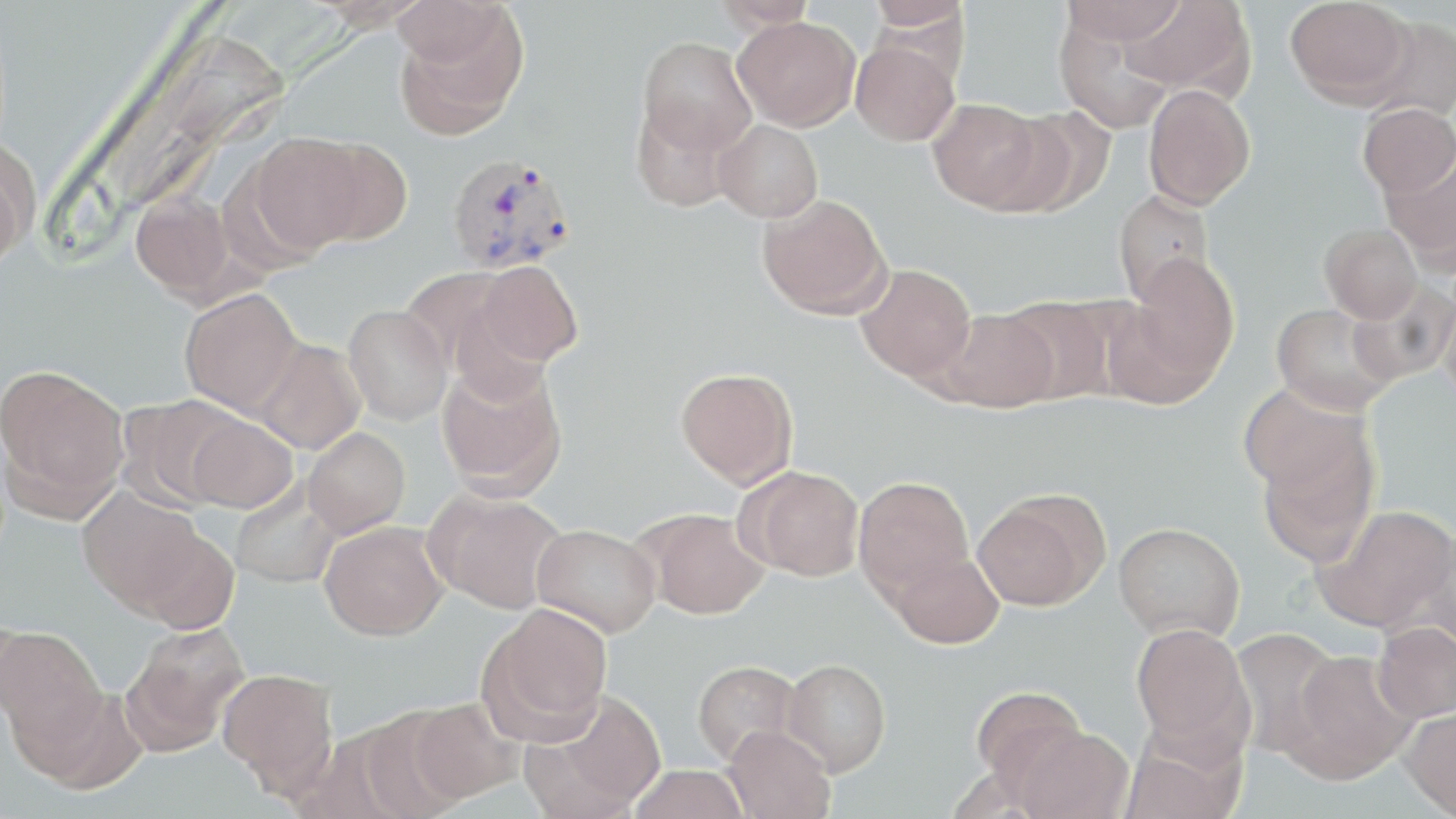

Summary:
  - Coordinate format: approximate bounding boxes as [x1, y1, x2, y2] in pixels
  - Uninfected red blood cell locations: [310, 0, 432, 31], [712, 0, 816, 30], [865, 0, 971, 31], [1061, 0, 1187, 45], [1122, 0, 1255, 97], [1284, 0, 1411, 104], [393, 5, 528, 140], [1359, 15, 1456, 123], [733, 16, 860, 131], [1055, 17, 1175, 134], [637, 36, 757, 155], [851, 39, 959, 146], [1143, 84, 1256, 210], [927, 98, 1044, 211], [631, 100, 738, 212], [1358, 103, 1456, 198], [1000, 106, 1117, 217], [714, 119, 823, 223], [249, 133, 373, 252], [303, 135, 413, 246], [0, 140, 38, 266], [1380, 152, 1456, 269], [215, 162, 326, 275], [1113, 190, 1215, 305], [130, 191, 238, 302], [757, 192, 892, 319], [1320, 223, 1423, 323], [1129, 253, 1239, 383], [475, 261, 582, 367], [856, 264, 976, 383], [399, 267, 519, 373], [1345, 280, 1456, 386], [179, 288, 304, 418], [1440, 289, 1456, 406], [1000, 296, 1118, 405], [1102, 297, 1223, 411], [1271, 303, 1398, 416], [343, 304, 453, 425], [937, 309, 1059, 413], [252, 339, 366, 454], [436, 358, 568, 499], [0, 364, 130, 513], [676, 367, 798, 489], [1239, 383, 1372, 501], [120, 394, 247, 511], [184, 413, 297, 514], [303, 427, 410, 538], [1255, 428, 1380, 568], [742, 466, 865, 581], [854, 476, 974, 601], [231, 481, 342, 589], [77, 485, 206, 615], [426, 491, 568, 613], [972, 492, 1107, 611], [1317, 503, 1456, 632], [642, 509, 768, 619], [319, 521, 448, 640], [1113, 522, 1244, 642], [532, 524, 661, 637], [135, 528, 241, 634], [890, 551, 1004, 648], [478, 604, 612, 741], [1372, 621, 1456, 723], [121, 623, 249, 755], [1130, 623, 1253, 753], [0, 624, 107, 759], [1229, 627, 1345, 758], [1284, 649, 1417, 784], [783, 659, 891, 776], [692, 660, 800, 765], [217, 668, 339, 795], [971, 685, 1092, 795], [539, 691, 666, 813], [409, 697, 524, 803], [351, 707, 468, 819], [1399, 708, 1456, 818], [722, 724, 836, 819], [1012, 727, 1133, 819], [1119, 730, 1248, 819], [629, 764, 749, 819]
  - Plasmodium vivax-infected red blood cell locations: [446, 152, 576, 275]
  - Slide-level diagnosis: Plasmodium vivax
  - Preparation: thin blood film
  - Modality: optical microscopy
  - Stain: May-Grünwald-Giemsa
  - Image size: 1456×819 pixels
  - Field of view: one of a larger specimen
  - Magnification: 1000x